Identify the parasite.
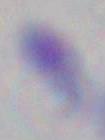

Toxoplasma gondii.

{
  "modality": "photomicrograph",
  "magnification": "1000x"
}